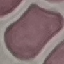

Result: no malaria parasites detected. Automatically extracted cell patch, resized to 64 × 64 pixels. Giemsa-stained preparation. Photographed with a smartphone camera at the microscope eyepiece. Thin blood smear.